Assess this cell for malaria.
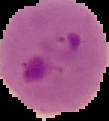

Parasitized.

Image is 109×121 pixels. Segmented cell region on a black background. From a thin blood film.